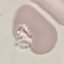

Result: no malaria parasites seen. Acquired by smartphone through the microscope eyepiece. Giemsa stain. Thin blood film. Cell patch, automatically extracted from a larger field of view and resized to 64 × 64 pixels.